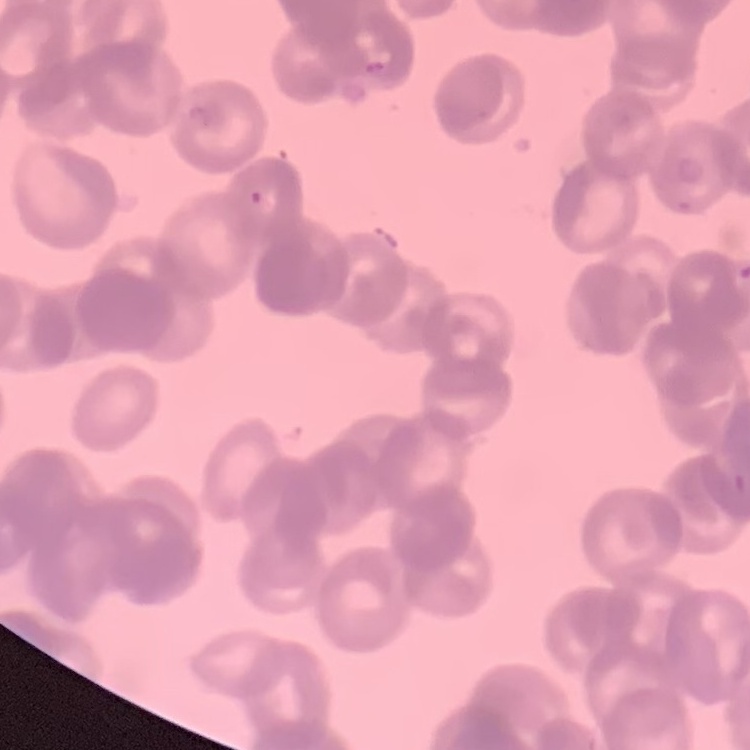 The erythrocytes exhibit rouleaux formation. Thin blood film. Field's or Giemsa stain. One tile cut from a larger photomicrograph.